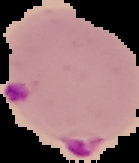

image type = segmented cell region with the area outside set to black
result = Plasmodium parasites identified
image size = 139×163 pixels
preparation = thin blood film